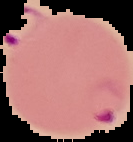

preparation: thin blood film
image_type: cell region segmented out of the field of view; surrounding area masked to black
result: malaria parasites detected
image_size: 133×142 pixels